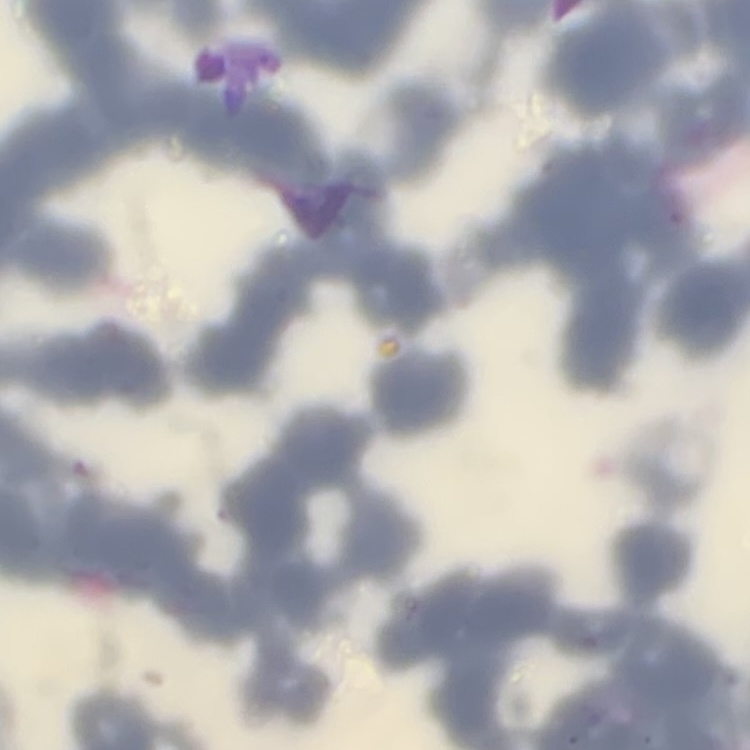

{
  "red_blood_cell_morphology": "rouleaux formation",
  "preparation": "thin blood smear",
  "image_type": "one tile cut from a larger photomicrograph",
  "stain": "Field's or Giemsa"
}